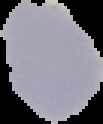

image type = segmented cell region on a black background
malaria status = uninfected
image size = 103×124 pixels
preparation = thin blood smear